Locate every blood parasite and identify its species.
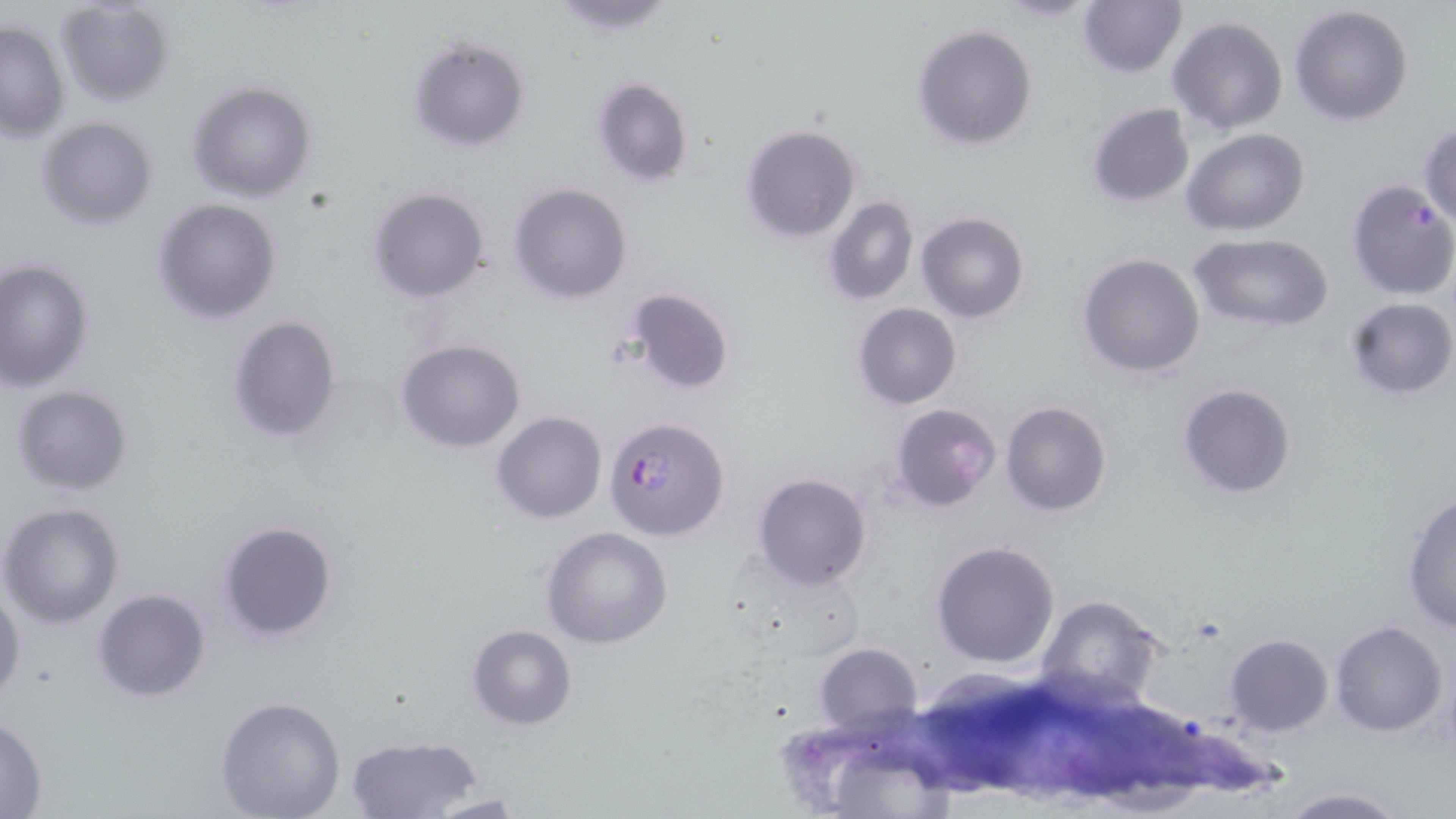

Approximate bounding boxes as (x1, y1, x2, y2) in pixels.
Plasmodium falciparum-infected red blood cells: (606, 415, 730, 541).
No Plasmodium ovale, Plasmodium malariae, Plasmodium vivax, Babesia divergens, or Trypanosoma brucei observed.

Summary:
  - Uninfected red blood cell locations: (53, 0, 177, 108), (544, 0, 679, 34), (1077, 0, 1187, 78), (1289, 5, 1414, 127), (1168, 14, 1288, 136), (0, 18, 70, 140), (914, 24, 1038, 150), (407, 35, 530, 150), (590, 74, 694, 188), (187, 80, 317, 203), (1086, 102, 1196, 207), (1085, 113, 1306, 221), (37, 117, 158, 229), (1418, 121, 1456, 230), (742, 125, 860, 243), (1182, 128, 1310, 236), (1346, 179, 1456, 299), (510, 182, 632, 303), (368, 186, 490, 302), (825, 195, 918, 305), (152, 198, 282, 323), (918, 212, 1029, 324), (1189, 233, 1334, 332), (1078, 252, 1205, 377), (0, 257, 95, 390), (624, 287, 735, 397), (1344, 298, 1454, 401), (854, 302, 961, 408), (228, 315, 342, 442), (397, 338, 526, 453), (1177, 382, 1297, 500), (10, 384, 134, 497), (1001, 400, 1110, 517), (891, 403, 1001, 515), (493, 411, 605, 524), (752, 471, 873, 591), (1401, 492, 1456, 633), (1, 501, 125, 628), (217, 518, 339, 642), (542, 526, 673, 648), (931, 539, 1060, 669), (0, 588, 24, 705), (93, 588, 211, 701), (1035, 594, 1165, 711), (1330, 620, 1448, 736), (467, 623, 577, 730), (1225, 633, 1332, 735), (813, 640, 922, 737), (214, 696, 347, 818), (0, 714, 48, 818), (345, 733, 486, 819), (1275, 787, 1410, 818), (424, 792, 535, 817)
  - Slide-level diagnosis: Plasmodium falciparum
  - Field of view: single
  - Preparation: thin blood film
  - Modality: optical microscopy
  - Image size: 1456×819 pixels
  - Stain: May-Grünwald-Giemsa
  - Magnification: 1000x